Assess this cell for malaria.
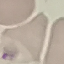
It is uninfected.

Acquired by smartphone through the microscope eyepiece. Giemsa-stained preparation. Thin blood smear. Automatically extracted cell patch, resized to 64 × 64 pixels.